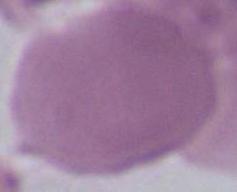
Summary:
  - Magnification: 1000x
  - Identification: erythrocyte
  - Modality: photomicrograph